Give the preparation type.
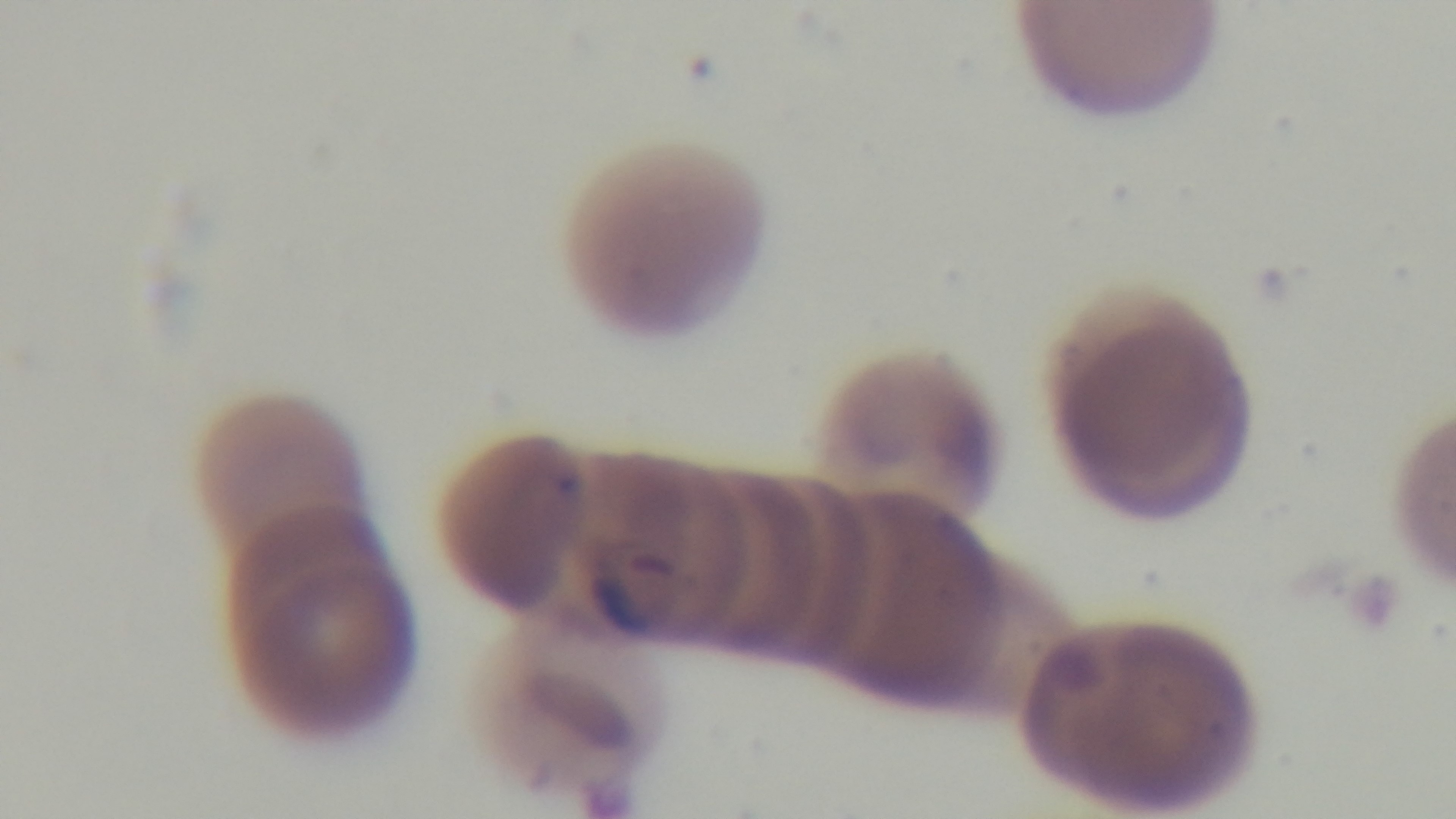

A thin smear.

Giemsa-stained. Mounted 4K digital camera. Malaria status: positive. Oil-immersion objective, 100x. Light microscopy. Single field of view.